Name the parasite shown.
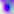
Toxoplasma gondii.

Micrograph. Captured at 400x magnification.